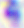
{
  "identification": "Toxoplasma gondii",
  "modality": "micrograph",
  "magnification": "400x"
}